Classify this cell by malaria status.
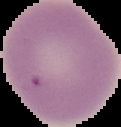
Uninfected.

The area outside the segmented cell region is set to black. From a thin blood film. Image is 121×127 pixels.